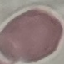
Summary:
  - Malaria status: uninfected
  - Stain: Giemsa
  - Image type: cell patch, automatically extracted from a larger field of view and resized to 64 × 64 pixels
  - Capture: smartphone camera at the microscope eyepiece
  - Preparation: thin blood smear